Report the malaria status of this cell.
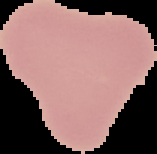

It is uninfected.

image size = 157×154 pixels
image type = cell region segmented out of the field of view; surrounding area masked to black
preparation = thin blood film